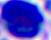

Summary:
  - Magnification: 400x
  - Modality: micrograph
  - Identification: white blood cell